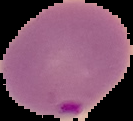

Summary:
  - Image size: 133×121 pixels
  - Preparation: thin blood film
  - Malaria status: parasitized
  - Image type: segmented cell region on a black background